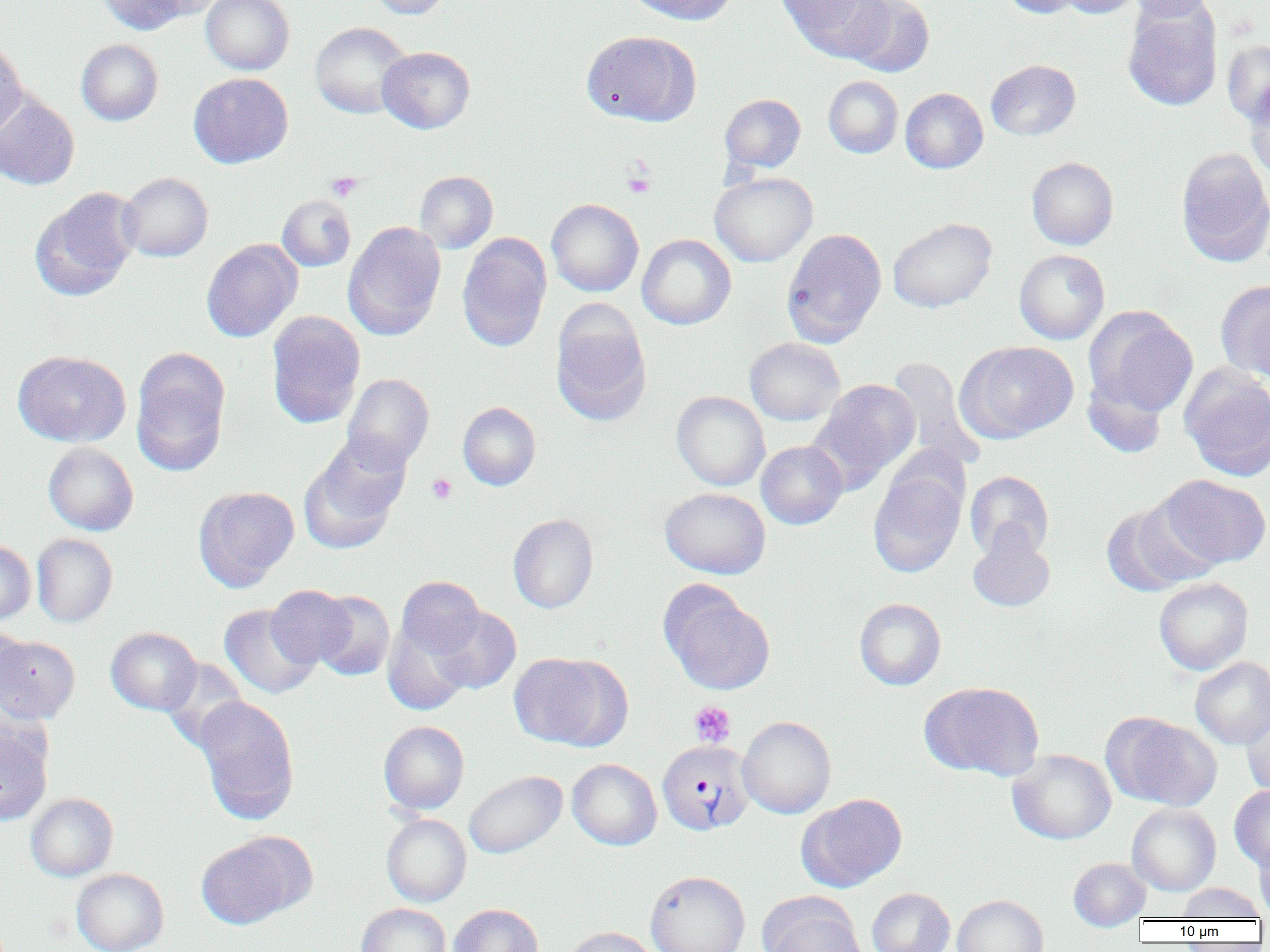

Summary:
  - Coordinate format: approximate bounding boxes as (x1,y1)-(x2,y2) corner pairs in pixels
  - Uninfected red blood cell locations: (96,0)-(189,34), (143,0)-(228,21), (201,0)-(294,75), (367,0)-(452,19), (624,0)-(736,25), (780,0)-(891,61), (844,0)-(935,78), (999,0)-(1085,18), (1057,0)-(1143,18), (1123,0)-(1218,20), (1122,2)-(1223,111), (310,22)-(412,119), (581,30)-(701,127), (0,37)-(27,140), (76,39)-(163,125), (1221,39)-(1270,127), (377,46)-(475,134), (986,60)-(1081,141), (189,72)-(293,168), (823,75)-(903,158), (1244,82)-(1270,180), (900,88)-(988,173), (0,92)-(80,190), (720,93)-(806,173), (1175,147)-(1270,267), (1027,157)-(1119,250), (415,171)-(498,253), (119,172)-(213,262), (710,172)-(817,267), (30,187)-(141,301), (277,195)-(356,272), (546,198)-(644,297), (887,217)-(997,313), (343,221)-(446,340), (781,228)-(887,347), (457,234)-(552,351), (637,234)-(736,330), (201,238)-(303,342), (1014,249)-(1110,344), (1215,280)-(1270,380), (550,306)-(651,426), (1083,306)-(1198,417), (266,311)-(366,428), (744,337)-(845,426), (956,341)-(1078,443), (12,350)-(131,447), (131,350)-(231,475), (886,357)-(985,472), (1179,364)-(1270,482), (1082,369)-(1269,468), (342,373)-(434,472), (1082,373)-(1169,458), (811,379)-(920,488), (672,391)-(770,491), (458,402)-(541,490), (298,438)-(410,554), (756,440)-(848,529), (43,442)-(138,535), (868,465)-(967,577), (965,470)-(1054,560), (1157,474)-(1269,569), (193,486)-(299,591), (660,487)-(771,579), (1101,499)-(1215,596), (508,513)-(598,613), (967,529)-(1055,612), (31,533)-(118,627), (0,540)-(36,625), (394,576)-(486,663), (1154,577)-(1253,675), (659,581)-(775,696), (266,585)-(356,668), (311,590)-(395,681), (854,598)-(946,690), (219,603)-(321,699), (428,604)-(522,695), (382,620)-(474,716), (1,626)-(32,711), (105,627)-(201,715), (0,635)-(80,723), (508,652)-(626,750), (1190,657)-(1270,748), (160,659)-(250,752), (920,681)-(1044,781), (194,696)-(300,825), (1241,703)-(1270,797), (1104,713)-(1221,811), (737,716)-(836,818), (379,720)-(469,814), (0,723)-(53,827), (1008,749)-(1116,845), (567,758)-(662,850), (464,770)-(567,859), (1229,785)-(1270,870), (26,793)-(119,881), (798,793)-(907,892), (1127,803)-(1221,896), (382,814)-(471,907), (196,832)-(312,930), (1253,832)-(1270,921), (1068,857)-(1150,931), (71,868)-(169,952), (645,871)-(751,952), (1177,883)-(1266,921), (866,888)-(955,952), (760,894)-(866,952), (953,895)-(1048,952), (356,903)-(451,952), (448,904)-(543,952), (561,927)-(661,952)
  - Plasmodium vivax-infected red blood cell locations: (657,740)-(755,836)
  - Platelet locations: (623,171)-(655,197), (326,172)-(363,201), (426,473)-(457,504), (689,700)-(735,746)
  - Slide-level diagnosis: Plasmodium vivax
  - Image size: 1270×952 pixels
  - Magnification: 1000x
  - Field of view: one of a larger specimen
  - Preparation: thin blood film
  - Modality: optical microscopy